State the preparation type.
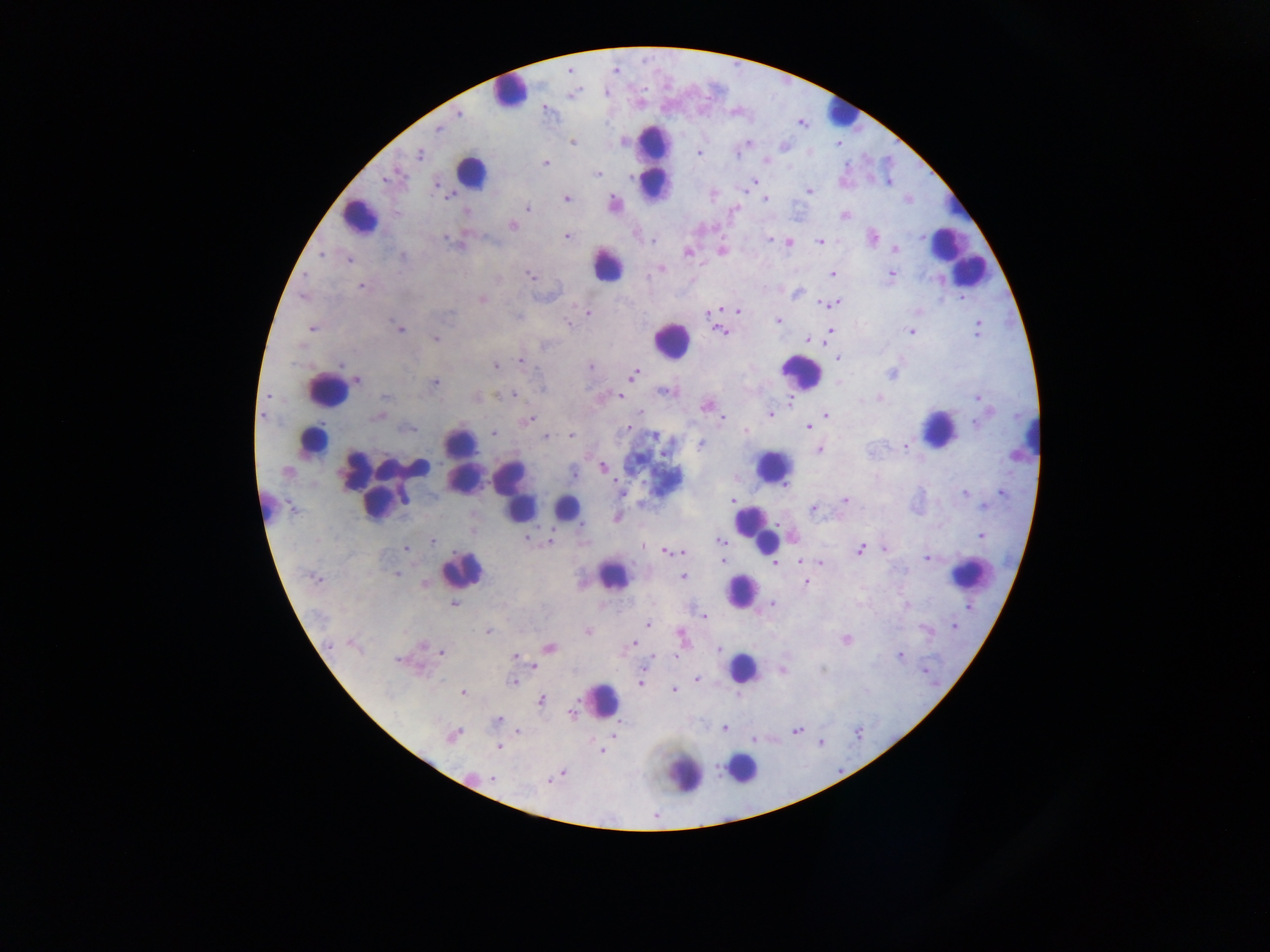

This is a thick smear.

Approximate centers as [x, y] in pixels. Leukocyte locations: [509, 91], [841, 113], [654, 161], [470, 172], [359, 217], [960, 258], [608, 264], [671, 340], [801, 371], [325, 389], [938, 428], [314, 439], [461, 441], [773, 467], [399, 468], [513, 488], [377, 504], [566, 507], [519, 508], [264, 509], [755, 527], [764, 539], [462, 569], [969, 573], [614, 576], [742, 590], [742, 667], [603, 699], [742, 768], [686, 774]. Plasmodium parasite locations: [615, 69], [458, 113], [439, 128], [572, 143], [749, 143], [783, 146], [699, 153], [420, 154], [736, 154], [765, 160], [546, 163], [598, 173], [756, 182], [437, 185], [809, 191], [449, 196], [566, 198], [765, 199], [907, 199], [614, 203], [528, 208], [734, 210], [465, 212], [844, 216], [512, 226], [567, 237], [874, 237], [770, 239], [654, 240], [450, 242], [820, 242], [790, 243], [894, 250], [687, 252], [721, 252], [321, 254], [402, 256], [349, 260], [661, 269], [833, 274], [891, 274], [529, 275], [649, 275], [362, 286], [797, 294], [482, 299], [834, 303], [827, 304], [737, 310], [711, 312], [450, 313], [588, 314], [518, 317], [778, 320], [567, 323], [979, 323], [312, 329], [399, 330], [977, 330], [720, 331], [830, 331], [910, 332], [828, 335], [435, 339], [807, 340], [544, 346], [838, 358], [520, 361], [340, 365], [495, 366], [590, 366], [634, 374], [891, 374], [357, 381], [435, 382], [664, 391], [513, 394], [385, 397], [620, 397], [878, 397], [978, 398], [790, 401], [706, 405], [639, 413], [771, 413], [263, 415], [826, 415], [377, 417], [530, 419], [722, 419], [977, 424], [808, 427], [409, 429], [745, 431], [493, 433], [570, 435], [546, 436], [653, 436], [701, 443], [905, 446], [819, 450], [603, 467], [287, 471], [574, 473], [1003, 492], [621, 493], [964, 493], [403, 497], [732, 500], [845, 500], [983, 507], [813, 508], [582, 524], [981, 536], [528, 539], [433, 541], [551, 541], [720, 541], [642, 547], [405, 548], [860, 549], [884, 549], [666, 552], [675, 553], [681, 553], [927, 558], [723, 561], [799, 561], [776, 563], [821, 563], [398, 574], [684, 577], [315, 578], [806, 582], [773, 604], [453, 605], [906, 605], [968, 606], [704, 616], [648, 624], [954, 627], [926, 629], [488, 632], [588, 632], [681, 636], [846, 640], [331, 643], [634, 643], [422, 645], [549, 648], [718, 649], [442, 652], [515, 656], [899, 656], [652, 658], [397, 659], [534, 667], [925, 670], [782, 671], [697, 679], [512, 682], [640, 682], [674, 690], [463, 692], [541, 700], [572, 713], [498, 720], [724, 729], [797, 730], [519, 732], [613, 735], [452, 736], [754, 740], [499, 747], [602, 751], [562, 773], [492, 779], [551, 779], [655, 815]. Single field of view. Image is 1270×952 pixels. Photographed through a microscope with a mobile-phone camera. Sample from Ghana.